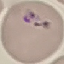

result: malaria parasites detected
preparation: thin smear
image_type: cell patch, automatically extracted from a larger field of view and resized to 64 × 64 pixels
stain: Giemsa
capture: smartphone through the microscope eyepiece